Name the parasite shown.
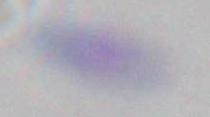
Toxoplasma gondii.

Summary:
  - Modality: photomicrograph
  - Magnification: 1000x